Identify the parasite.
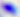

This is Toxoplasma gondii.

{
  "modality": "photomicrograph",
  "magnification": "400x"
}